Report the malaria status of this cell.
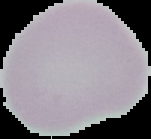
It is uninfected.

Summary:
  - Preparation: thin blood smear
  - Image type: cell region segmented out of the field of view; surrounding area masked to black
  - Image size: 151×139 pixels